Classify this cell by malaria status.
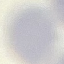
Uninfected.

Summary:
  - Stain: Giemsa
  - Capture: smartphone through the microscope eyepiece
  - Image type: automatically extracted cell patch, resized to 64 × 64 pixels
  - Preparation: thin blood film